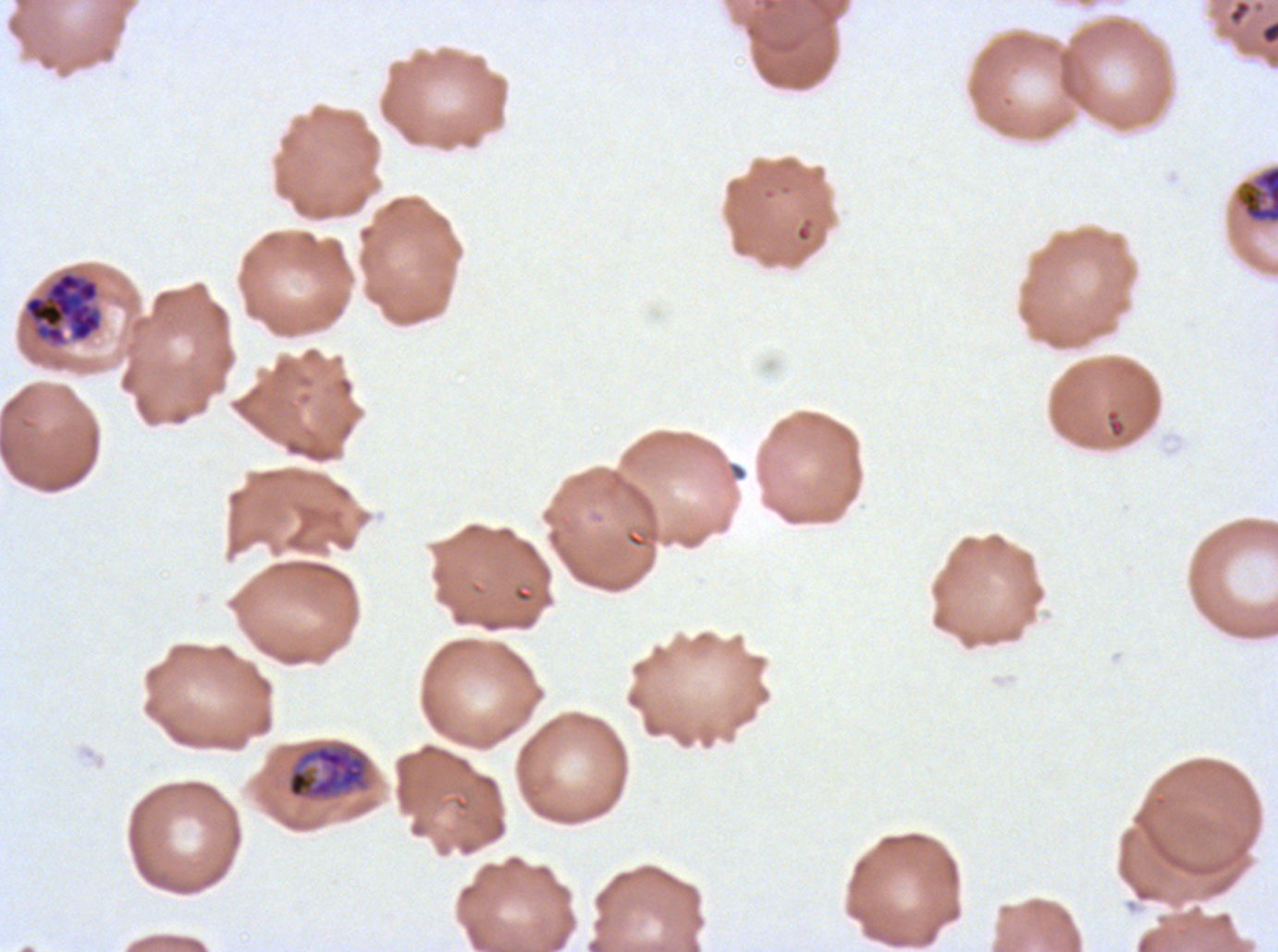

Approximate bounding boxes as [x1, y1, x2, y2] in pixels.
Summary:
  - Debris locations: [1228, 0, 1252, 25]
  - Late schizont locations: [21, 269, 104, 350]
  - Mid trophozoite locations: [1234, 165, 1277, 225]
  - Early schizont locations: [286, 743, 369, 799]
  - Specimen: ex-vivo P. falciparum culture from a patient in The Gambia, grown for 24 to 48 hours
  - Field of view: one sub-image of a larger composite
  - Preparation: thin blood smear
  - Life-cycle stages observed: mid trophozoite, early schizont, late schizont
  - Stain: Giemsa
  - Image size: 1278×952 pixels